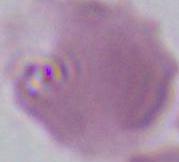 Captured at 1000x magnification. A red blood cell is shown. Photomicrograph.